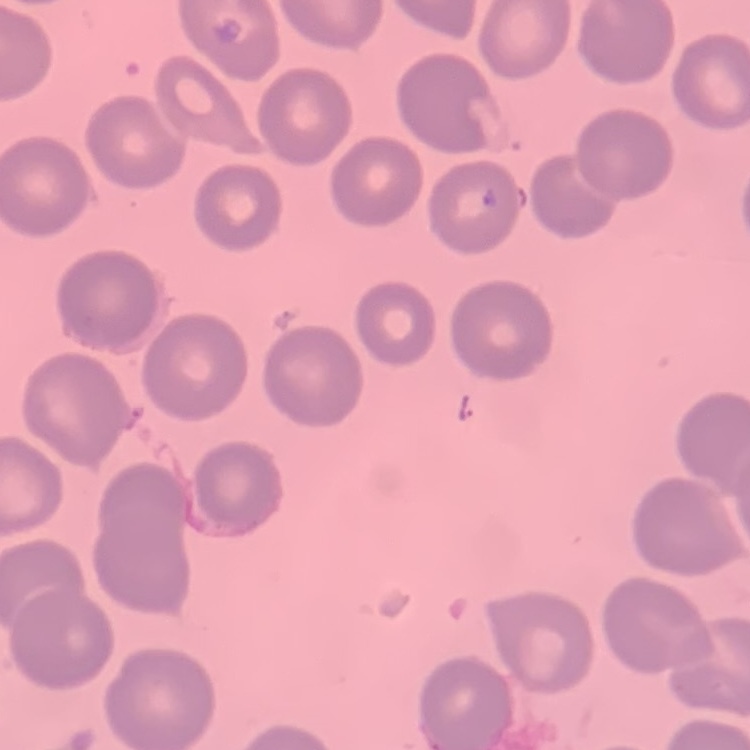 The red blood cells exhibit no rouleaux formation. One tile cut from a larger photomicrograph. Thin blood smear. Field's or Giemsa stain.